Name the parasite shown.
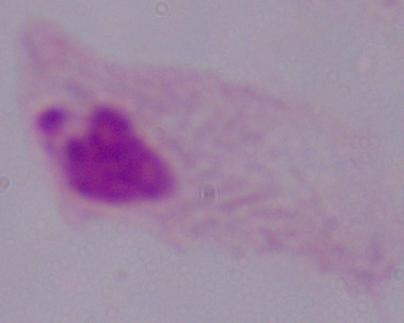
This is a trichomonad.

Captured at 1000x magnification. Micrograph.